Give the extent of all Plasmodium falciparum-infected red blood cells.
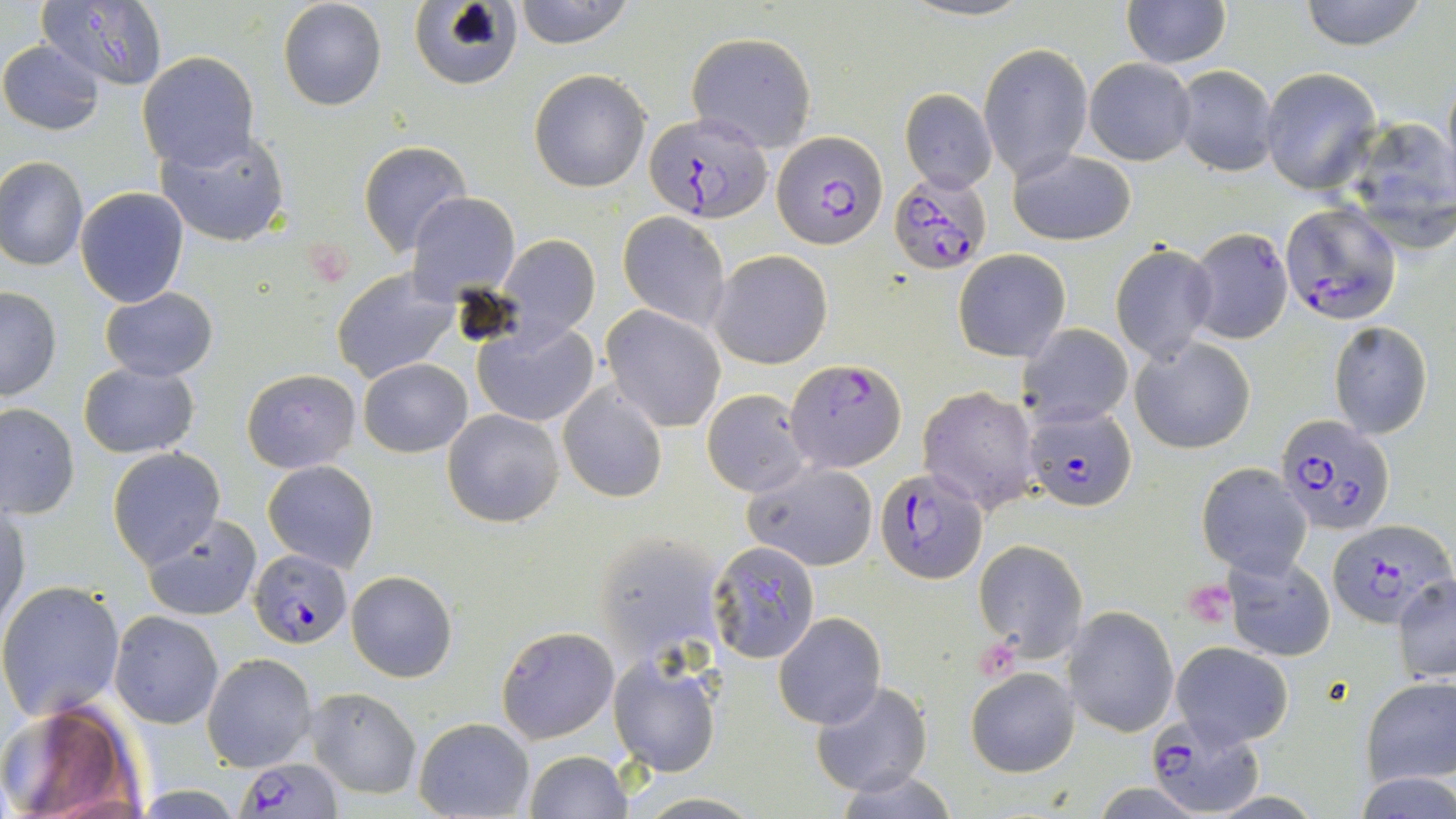

Approximate bounding boxes as named x1/y1/x2/y2 corners in pixels.
Plasmodium falciparum-infected red blood cells: (x1=641, y1=113, x2=773, y2=224), (x1=771, y1=129, x2=887, y2=247), (x1=889, y1=170, x2=992, y2=275), (x1=1279, y1=202, x2=1402, y2=324), (x1=784, y1=358, x2=907, y2=472), (x1=1026, y1=406, x2=1135, y2=510), (x1=1276, y1=414, x2=1396, y2=535), (x1=876, y1=468, x2=986, y2=585), (x1=1325, y1=517, x2=1452, y2=630), (x1=249, y1=549, x2=352, y2=648), (x1=1143, y1=711, x2=1263, y2=816), (x1=239, y1=756, x2=341, y2=817).

Platelet locations: (x1=1183, y1=579, x2=1236, y2=626). Uninfected red blood cell locations: (x1=37, y1=0, x2=171, y2=93), (x1=278, y1=0, x2=387, y2=112), (x1=410, y1=0, x2=524, y2=89), (x1=512, y1=0, x2=637, y2=48), (x1=1120, y1=0, x2=1231, y2=68), (x1=1297, y1=0, x2=1429, y2=51), (x1=686, y1=31, x2=817, y2=150), (x1=0, y1=39, x2=104, y2=134), (x1=979, y1=42, x2=1092, y2=181), (x1=138, y1=52, x2=258, y2=172), (x1=1084, y1=57, x2=1196, y2=165), (x1=1171, y1=65, x2=1279, y2=175), (x1=1441, y1=67, x2=1455, y2=191), (x1=528, y1=68, x2=651, y2=193), (x1=1259, y1=68, x2=1382, y2=193), (x1=900, y1=89, x2=997, y2=193), (x1=1336, y1=116, x2=1456, y2=247), (x1=154, y1=129, x2=291, y2=248), (x1=359, y1=141, x2=470, y2=255), (x1=1009, y1=149, x2=1137, y2=245), (x1=0, y1=156, x2=88, y2=271), (x1=74, y1=187, x2=191, y2=309), (x1=407, y1=192, x2=521, y2=305), (x1=618, y1=212, x2=730, y2=330), (x1=1185, y1=228, x2=1293, y2=344), (x1=498, y1=233, x2=600, y2=339), (x1=1109, y1=244, x2=1218, y2=364), (x1=954, y1=248, x2=1071, y2=362), (x1=709, y1=249, x2=833, y2=369), (x1=331, y1=267, x2=458, y2=383), (x1=99, y1=287, x2=218, y2=381), (x1=0, y1=288, x2=62, y2=402), (x1=602, y1=306, x2=725, y2=432), (x1=474, y1=320, x2=599, y2=426), (x1=1328, y1=320, x2=1434, y2=440), (x1=1017, y1=324, x2=1134, y2=425), (x1=1131, y1=337, x2=1256, y2=454), (x1=360, y1=357, x2=471, y2=457), (x1=78, y1=361, x2=200, y2=459), (x1=242, y1=367, x2=360, y2=473), (x1=557, y1=381, x2=668, y2=503), (x1=918, y1=384, x2=1042, y2=514), (x1=702, y1=389, x2=814, y2=497), (x1=1, y1=403, x2=79, y2=519), (x1=443, y1=409, x2=565, y2=527), (x1=108, y1=448, x2=227, y2=568), (x1=263, y1=460, x2=379, y2=572), (x1=745, y1=462, x2=878, y2=571), (x1=1197, y1=463, x2=1312, y2=576), (x1=1, y1=504, x2=29, y2=633), (x1=142, y1=514, x2=263, y2=620), (x1=592, y1=531, x2=728, y2=662), (x1=973, y1=539, x2=1086, y2=662), (x1=707, y1=542, x2=821, y2=664), (x1=1224, y1=550, x2=1335, y2=663), (x1=346, y1=571, x2=458, y2=681), (x1=1392, y1=574, x2=1456, y2=681), (x1=0, y1=582, x2=127, y2=720), (x1=1067, y1=606, x2=1179, y2=738), (x1=110, y1=611, x2=223, y2=729), (x1=774, y1=613, x2=885, y2=729), (x1=495, y1=626, x2=619, y2=743), (x1=1170, y1=643, x2=1294, y2=745), (x1=203, y1=653, x2=317, y2=773), (x1=608, y1=653, x2=720, y2=778), (x1=966, y1=667, x2=1079, y2=777), (x1=1359, y1=676, x2=1456, y2=786), (x1=810, y1=682, x2=932, y2=797), (x1=308, y1=687, x2=421, y2=799), (x1=0, y1=703, x2=142, y2=818), (x1=413, y1=717, x2=533, y2=819), (x1=524, y1=749, x2=630, y2=818), (x1=839, y1=773, x2=957, y2=818), (x1=1355, y1=774, x2=1456, y2=818), (x1=633, y1=793, x2=765, y2=818). Slide-level diagnosis: Plasmodium falciparum. Captured at 1000x magnification. Thin blood smear. Image is 1456×819 pixels. Single field of view. May-Grünwald-Giemsa stain. Optical microscopy.